Assess this cell for malaria.
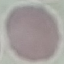

It is uninfected.

stain = Giemsa
image type = cell patch, automatically extracted from a larger field of view and resized to 64 × 64 pixels
preparation = thin blood film
capture = smartphone through the microscope eyepiece